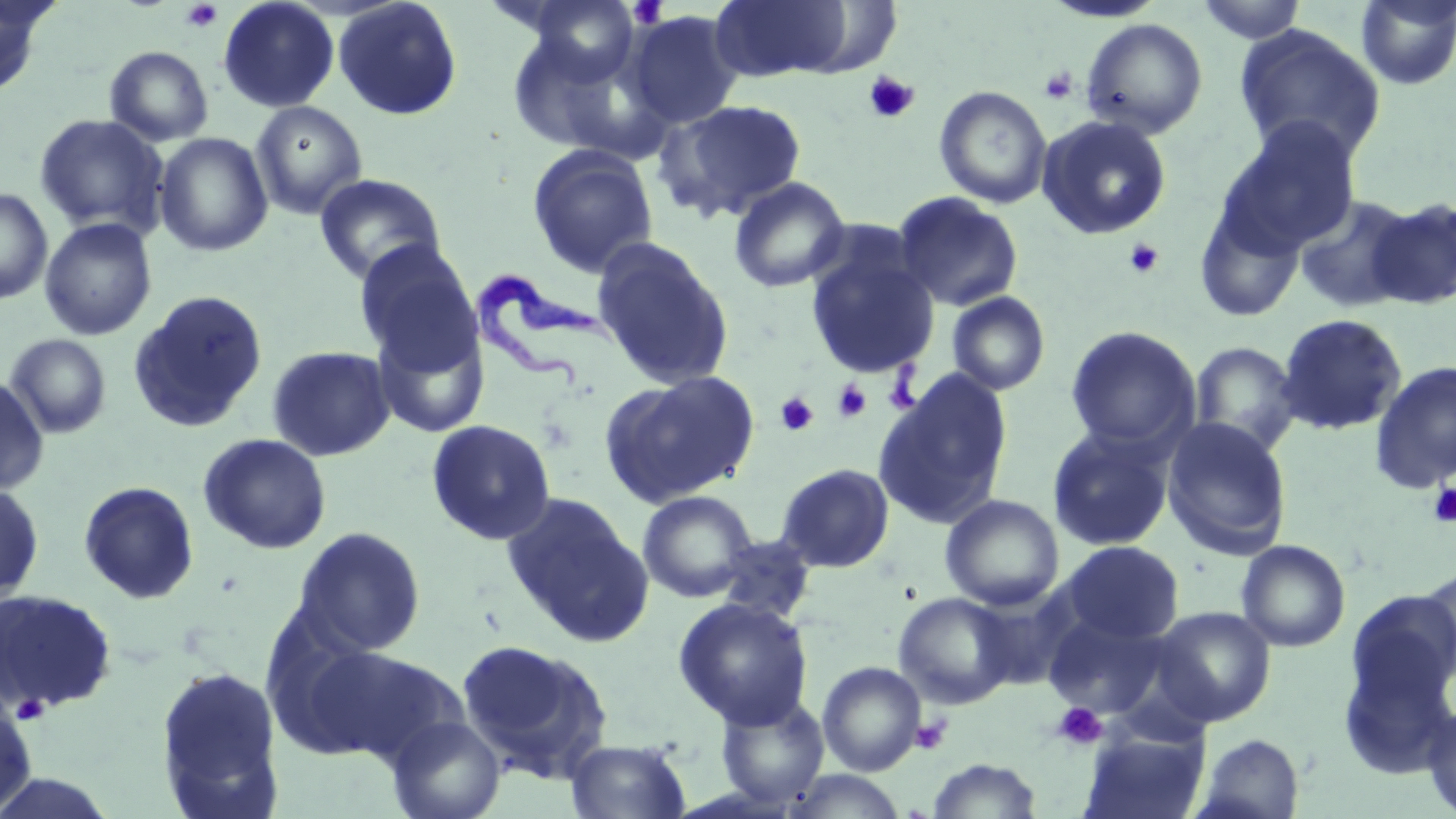
slide_level_diagnosis: Trypanosoma brucei
platelet_locations: 'approximate bounding boxes as named x1/y1/x2/y2 corners in pixels: (x1=627, y1=0, x2=669, y2=29), (x1=180, y1=1, x2=223, y2=33), (x1=1038, y1=67, x2=1078, y2=104), (x1=862, y1=70, x2=921, y2=124), (x1=1123, y1=239, x2=1165, y2=279), (x1=833, y1=380, x2=871, y2=423), (x1=776, y1=392, x2=818, y2=436), (x1=1427, y1=482, x2=1456, y2=527), (x1=12, y1=693, x2=49, y2=725), (x1=1053, y1=703, x2=1107, y2=750), (x1=912, y1=715, x2=951, y2=754)'
image_size: 1456×819 pixels
field_of_view: single
stain: May-Grünwald-Giemsa
trypanosoma_brucei_locations: 'approximate bounding boxes as named x1/y1/x2/y2 corners in pixels: (x1=463, y1=268, x2=616, y2=389)'
modality: light microscopy
uninfected_red_blood_cell_locations: 'approximate bounding boxes as named x1/y1/x2/y2 corners in pixels: (x1=0, y1=0, x2=58, y2=96), (x1=218, y1=0, x2=340, y2=113), (x1=332, y1=0, x2=462, y2=120), (x1=522, y1=0, x2=643, y2=86), (x1=708, y1=0, x2=856, y2=82), (x1=1040, y1=0, x2=1169, y2=24), (x1=1194, y1=0, x2=1310, y2=44), (x1=1354, y1=0, x2=1456, y2=90), (x1=624, y1=11, x2=743, y2=129), (x1=1080, y1=18, x2=1208, y2=139), (x1=1234, y1=24, x2=1388, y2=166), (x1=504, y1=29, x2=637, y2=157), (x1=105, y1=46, x2=213, y2=146), (x1=934, y1=86, x2=1053, y2=210), (x1=655, y1=99, x2=807, y2=221), (x1=250, y1=101, x2=368, y2=220), (x1=34, y1=114, x2=169, y2=237), (x1=1037, y1=114, x2=1173, y2=241), (x1=1217, y1=118, x2=1363, y2=254), (x1=154, y1=132, x2=273, y2=256), (x1=527, y1=144, x2=658, y2=278), (x1=315, y1=173, x2=447, y2=287), (x1=728, y1=176, x2=851, y2=293), (x1=0, y1=188, x2=53, y2=305), (x1=892, y1=192, x2=1024, y2=311), (x1=1293, y1=194, x2=1420, y2=313), (x1=1365, y1=196, x2=1456, y2=310), (x1=1193, y1=198, x2=1306, y2=323), (x1=39, y1=217, x2=157, y2=341), (x1=591, y1=238, x2=734, y2=391), (x1=353, y1=241, x2=481, y2=372), (x1=805, y1=247, x2=940, y2=379), (x1=128, y1=290, x2=269, y2=433), (x1=946, y1=291, x2=1051, y2=396), (x1=1275, y1=313, x2=1408, y2=436), (x1=372, y1=321, x2=489, y2=439), (x1=1064, y1=326, x2=1201, y2=453), (x1=4, y1=333, x2=112, y2=438), (x1=1189, y1=341, x2=1302, y2=454), (x1=267, y1=345, x2=396, y2=462), (x1=1369, y1=360, x2=1456, y2=493), (x1=600, y1=370, x2=760, y2=508), (x1=873, y1=372, x2=1013, y2=529), (x1=0, y1=375, x2=48, y2=495), (x1=1161, y1=416, x2=1292, y2=558), (x1=426, y1=419, x2=557, y2=545), (x1=1047, y1=426, x2=1175, y2=552), (x1=198, y1=433, x2=332, y2=554), (x1=776, y1=463, x2=894, y2=573), (x1=78, y1=480, x2=200, y2=604), (x1=0, y1=481, x2=44, y2=608), (x1=637, y1=490, x2=757, y2=603), (x1=501, y1=493, x2=653, y2=646), (x1=940, y1=494, x2=1065, y2=611), (x1=292, y1=526, x2=426, y2=656), (x1=714, y1=535, x2=817, y2=624), (x1=1236, y1=539, x2=1351, y2=652), (x1=1059, y1=540, x2=1184, y2=644), (x1=1417, y1=566, x2=1455, y2=680), (x1=0, y1=588, x2=118, y2=715), (x1=1341, y1=589, x2=1456, y2=753), (x1=893, y1=592, x2=1016, y2=709), (x1=673, y1=597, x2=814, y2=729), (x1=1153, y1=606, x2=1277, y2=726), (x1=1042, y1=613, x2=1169, y2=718), (x1=457, y1=638, x2=614, y2=782), (x1=297, y1=642, x2=460, y2=763), (x1=817, y1=661, x2=926, y2=776), (x1=154, y1=663, x2=285, y2=816), (x1=715, y1=693, x2=829, y2=809), (x1=0, y1=699, x2=38, y2=814), (x1=1421, y1=702, x2=1456, y2=818), (x1=386, y1=715, x2=505, y2=819), (x1=1081, y1=726, x2=1211, y2=819), (x1=1193, y1=733, x2=1305, y2=819), (x1=565, y1=737, x2=691, y2=818), (x1=926, y1=757, x2=1042, y2=818), (x1=783, y1=769, x2=911, y2=818)'
preparation: thin blood film
magnification: 1000x